Classify this cell by malaria status.
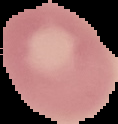
It is uninfected.

image_type: segmented cell region on a black background
image_size: 118×124 pixels
preparation: thin blood film